State the blood parasite species.
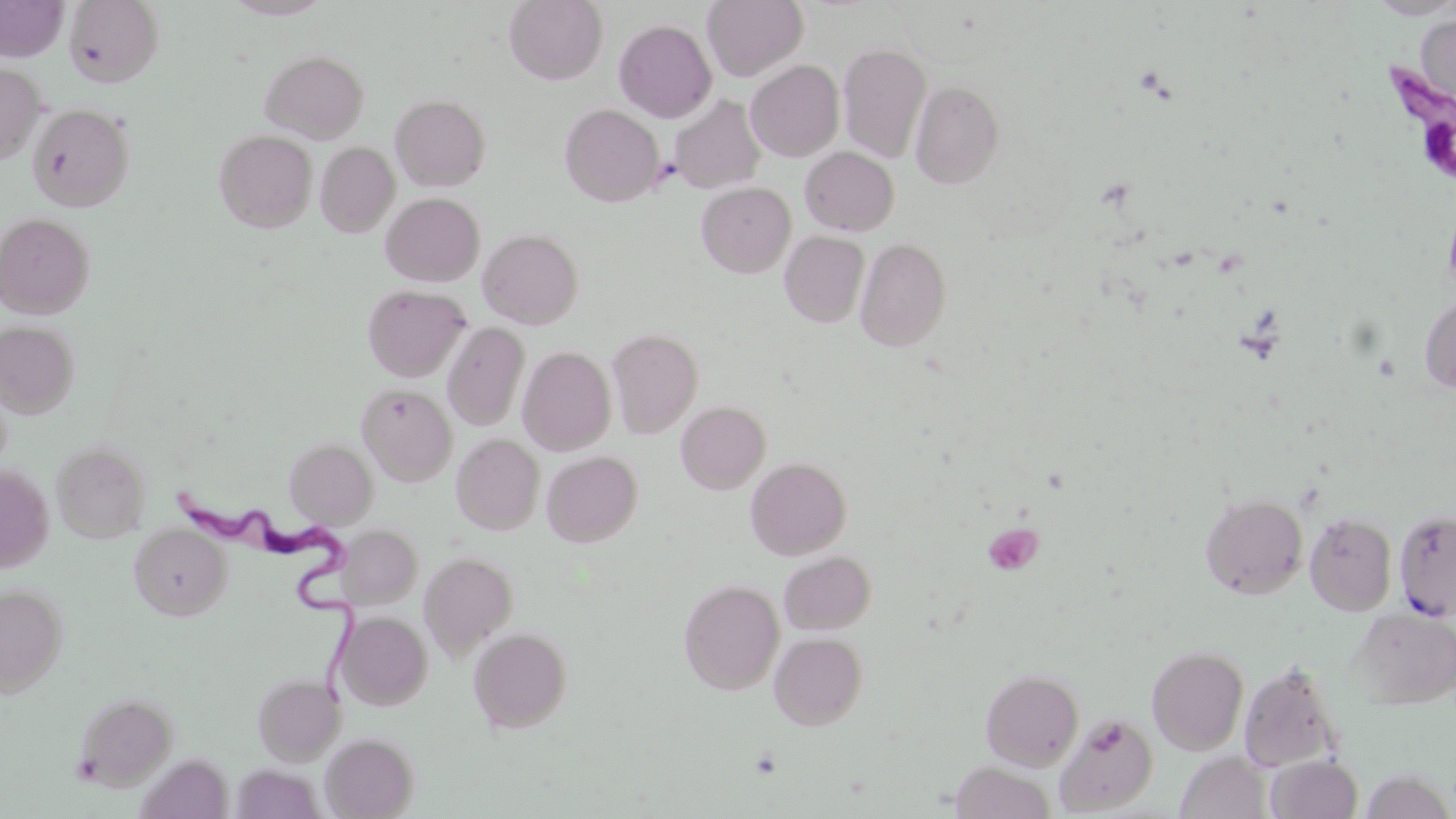

Trypanosoma brucei.

Approximate bounding boxes as named x1/y1/x2/y2 corners in pixels. Platelet locations: (x1=982, y1=523, x2=1043, y2=576). Uninfected red blood cell locations: (x1=0, y1=0, x2=67, y2=61), (x1=63, y1=0, x2=164, y2=87), (x1=223, y1=0, x2=334, y2=20), (x1=504, y1=0, x2=608, y2=84), (x1=1368, y1=0, x2=1456, y2=19), (x1=703, y1=1, x2=808, y2=81), (x1=1415, y1=11, x2=1456, y2=113), (x1=614, y1=19, x2=717, y2=123), (x1=838, y1=42, x2=931, y2=163), (x1=260, y1=49, x2=367, y2=143), (x1=746, y1=60, x2=844, y2=162), (x1=0, y1=63, x2=44, y2=165), (x1=910, y1=80, x2=1004, y2=189), (x1=391, y1=94, x2=491, y2=191), (x1=669, y1=94, x2=766, y2=194), (x1=27, y1=103, x2=134, y2=211), (x1=560, y1=104, x2=665, y2=207), (x1=214, y1=129, x2=316, y2=232), (x1=315, y1=142, x2=399, y2=238), (x1=800, y1=147, x2=899, y2=236), (x1=696, y1=182, x2=796, y2=277), (x1=381, y1=192, x2=485, y2=287), (x1=1443, y1=198, x2=1456, y2=302), (x1=0, y1=212, x2=95, y2=318), (x1=478, y1=228, x2=584, y2=328), (x1=780, y1=231, x2=869, y2=327), (x1=855, y1=237, x2=951, y2=352), (x1=362, y1=284, x2=471, y2=381), (x1=1419, y1=292, x2=1456, y2=394), (x1=0, y1=321, x2=80, y2=418), (x1=442, y1=322, x2=530, y2=431), (x1=606, y1=328, x2=703, y2=438), (x1=518, y1=346, x2=616, y2=455), (x1=357, y1=384, x2=456, y2=486), (x1=677, y1=401, x2=771, y2=494), (x1=452, y1=433, x2=544, y2=535), (x1=285, y1=439, x2=377, y2=527), (x1=52, y1=441, x2=150, y2=543), (x1=542, y1=450, x2=642, y2=547), (x1=746, y1=457, x2=851, y2=560), (x1=0, y1=464, x2=54, y2=572), (x1=1201, y1=492, x2=1308, y2=599), (x1=1394, y1=508, x2=1456, y2=620), (x1=1304, y1=512, x2=1397, y2=616), (x1=129, y1=523, x2=232, y2=620), (x1=339, y1=525, x2=421, y2=608), (x1=419, y1=551, x2=518, y2=661), (x1=779, y1=551, x2=876, y2=634), (x1=679, y1=579, x2=784, y2=695), (x1=0, y1=584, x2=67, y2=697), (x1=1351, y1=608, x2=1456, y2=710), (x1=337, y1=611, x2=432, y2=710), (x1=468, y1=627, x2=573, y2=732), (x1=769, y1=632, x2=868, y2=730), (x1=1147, y1=645, x2=1249, y2=755), (x1=1239, y1=661, x2=1344, y2=772), (x1=980, y1=668, x2=1084, y2=771), (x1=253, y1=673, x2=346, y2=765), (x1=73, y1=692, x2=178, y2=790), (x1=1055, y1=713, x2=1158, y2=815), (x1=321, y1=732, x2=419, y2=818), (x1=1175, y1=751, x2=1272, y2=819), (x1=1265, y1=755, x2=1363, y2=819), (x1=951, y1=760, x2=1056, y2=819), (x1=231, y1=763, x2=325, y2=819), (x1=1359, y1=770, x2=1455, y2=818). Trypanosoma brucei locations: (x1=1390, y1=65, x2=1455, y2=179), (x1=174, y1=482, x2=363, y2=703). Captured at 1000x magnification. May-Grünwald-Giemsa stain. Single field of view. Thin blood smear. Image is 1456×819 pixels. Light microscopy.